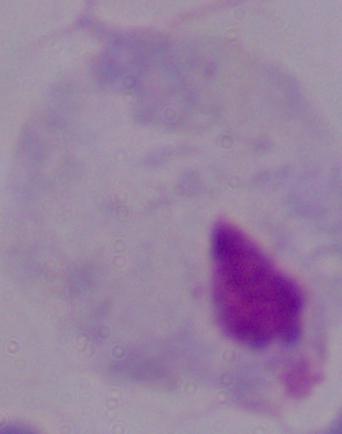
A trichomonad is seen. Captured at 1000x magnification. Micrograph.